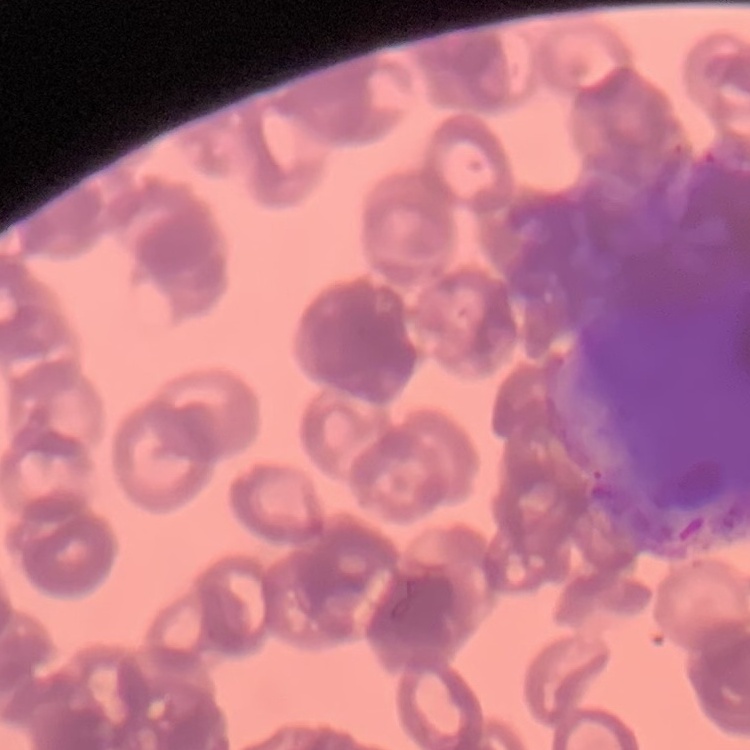

red blood cell morphology = rouleaux formation
image type = square crop of a larger photomicrograph
preparation = thin peripheral smear
stain = Field's or Giemsa